Identify the blood parasite species.
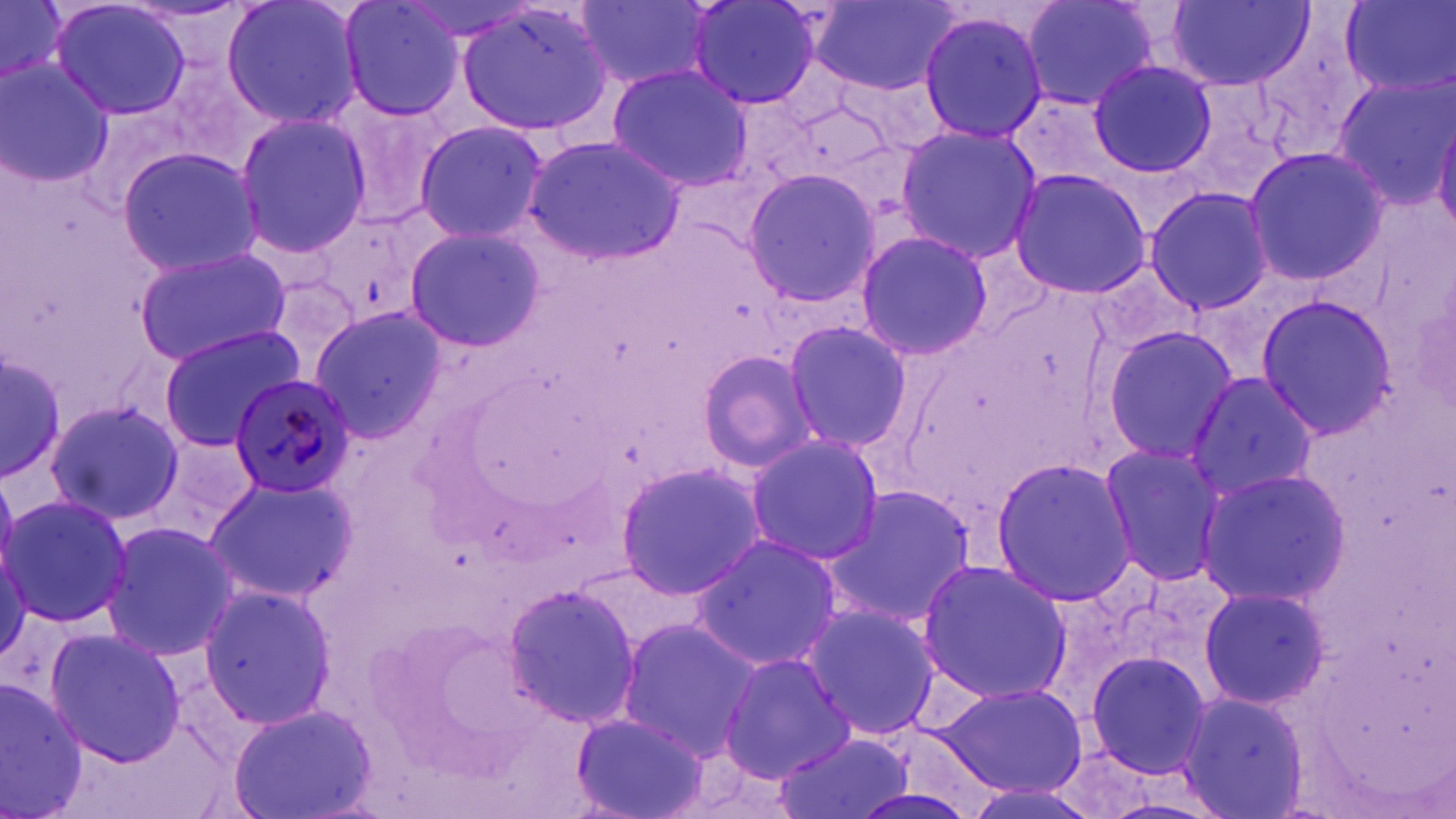
Plasmodium malariae.

image size = 1456×819 pixels
magnification = 1000x
Plasmodium malariae-infected red blood cell locations = approximate bounding boxes as (x1, y1, x2, y2) in pixels: (230, 372, 357, 497)
preparation = thin blood film
modality = light microscopy
uninfected red blood cell locations = approximate bounding boxes as (x1, y1, x2, y2) in pixels: (1, 0, 67, 86), (48, 0, 194, 121), (222, 0, 368, 131), (336, 0, 467, 120), (685, 0, 826, 111), (1021, 0, 1162, 111), (1169, 0, 1315, 90), (573, 1, 715, 88), (810, 1, 961, 94), (1342, 1, 1453, 98), (455, 2, 617, 138), (917, 9, 1051, 143), (1087, 60, 1217, 177), (0, 62, 112, 187), (606, 64, 753, 192), (1332, 77, 1456, 206), (331, 95, 460, 223), (232, 112, 374, 258), (1433, 117, 1456, 237), (413, 120, 549, 243), (894, 122, 1041, 264), (522, 135, 683, 264), (1242, 146, 1389, 285), (116, 147, 263, 277), (741, 167, 882, 308), (1008, 167, 1152, 300), (1142, 186, 1277, 315), (403, 225, 545, 353), (852, 230, 993, 359), (134, 246, 294, 367), (1252, 295, 1398, 438), (308, 305, 445, 441), (780, 318, 914, 452), (156, 326, 305, 449), (1099, 326, 1240, 465), (696, 348, 820, 472), (0, 354, 66, 483), (1186, 371, 1317, 505), (44, 399, 185, 525), (741, 432, 883, 566), (1096, 442, 1226, 584), (988, 455, 1137, 607), (615, 462, 769, 599), (1197, 466, 1351, 608), (201, 475, 355, 604), (822, 485, 979, 626), (3, 493, 132, 627), (100, 520, 237, 662), (693, 534, 845, 672), (915, 557, 1072, 704), (503, 583, 641, 728), (1196, 584, 1330, 711), (196, 585, 339, 728), (797, 603, 946, 745), (615, 619, 760, 757), (43, 629, 189, 766), (1078, 646, 1217, 784), (719, 652, 855, 783), (0, 680, 88, 818), (933, 682, 1086, 796), (1177, 687, 1308, 819), (231, 704, 377, 819), (570, 713, 710, 819), (773, 731, 916, 819)
stain = May-Grünwald-Giemsa
field of view = single